State the blood parasite species.
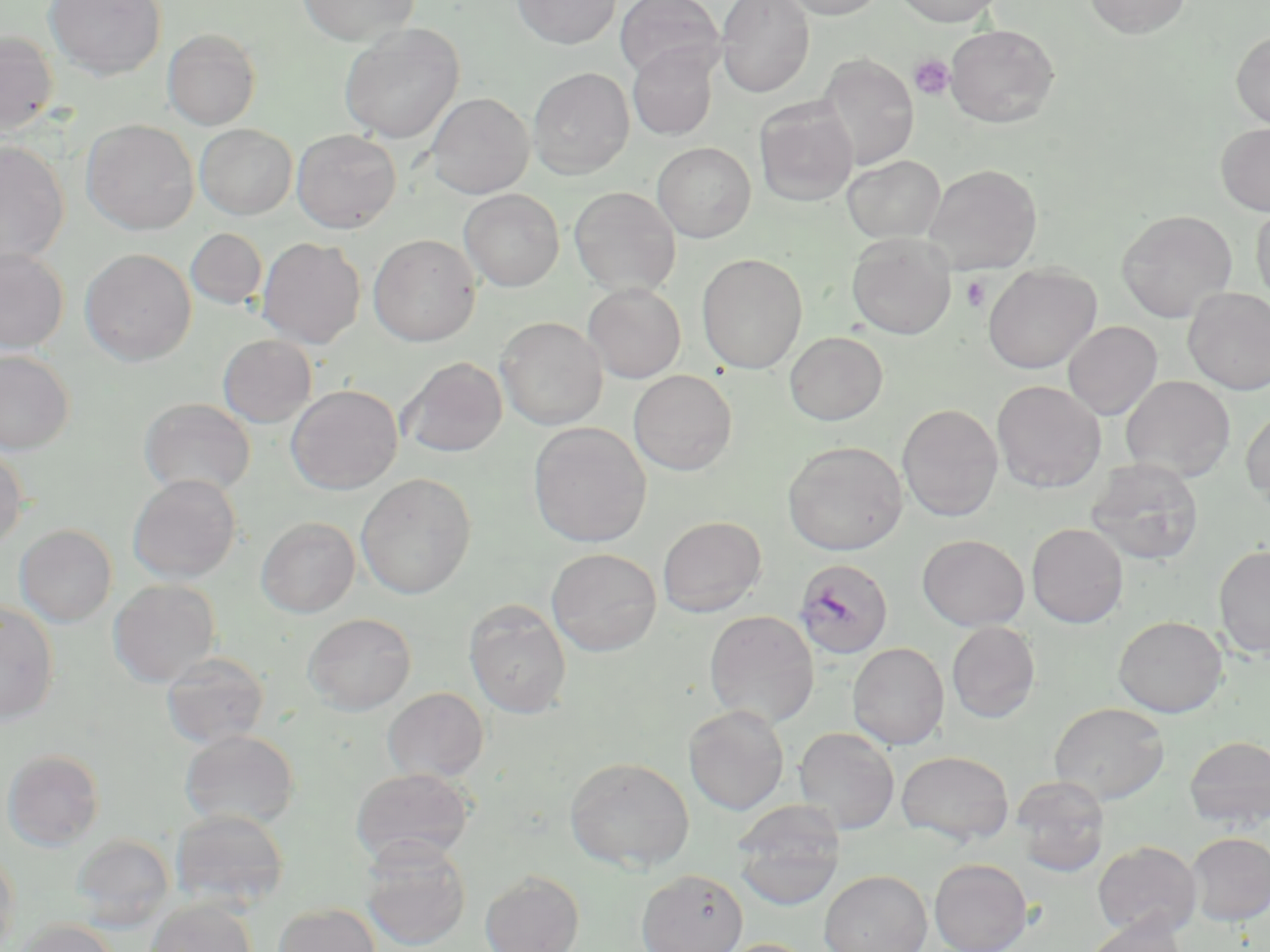

Plasmodium falciparum.

Approximate bounding boxes as (x1,y1)-(x2,y2) corner pairs in pixels. Plasmodium falciparum-infected red blood cell locations: (794,558)-(895,661). Platelet locations: (909,54)-(955,100), (961,275)-(991,313). Uninfected red blood cell locations: (44,0)-(166,80), (296,0)-(419,45), (513,0)-(620,49), (615,0)-(724,81), (715,0)-(815,97), (780,0)-(885,20), (894,0)-(1001,27), (1084,0)-(1192,38), (339,23)-(464,144), (944,24)-(1059,128), (163,28)-(261,130), (0,30)-(59,134), (1232,30)-(1270,129), (627,45)-(718,141), (815,54)-(920,170), (528,68)-(634,179), (426,92)-(534,199), (754,99)-(859,207), (81,119)-(199,235), (1216,122)-(1270,216), (195,124)-(297,220), (292,129)-(401,233), (0,140)-(69,265), (652,142)-(756,243), (843,155)-(945,242), (923,163)-(1042,274), (569,186)-(681,295), (459,189)-(564,292), (1251,200)-(1270,307), (1116,209)-(1237,322), (186,228)-(267,309), (846,233)-(957,339), (368,234)-(481,346), (256,236)-(366,348), (0,247)-(69,354), (80,248)-(197,365), (696,253)-(807,374), (983,263)-(1101,373), (583,283)-(686,383), (1184,287)-(1270,395), (496,316)-(607,430), (1063,321)-(1163,420), (784,331)-(888,425), (218,334)-(317,427), (0,349)-(74,454), (400,357)-(508,458), (628,370)-(737,475), (1120,375)-(1236,482), (992,380)-(1106,493), (286,384)-(403,494), (139,398)-(256,498), (897,404)-(1003,522), (1241,407)-(1270,509), (528,422)-(651,548), (782,440)-(907,556), (0,445)-(27,549), (1085,457)-(1204,566), (356,473)-(477,599), (127,474)-(242,583), (256,516)-(360,617), (657,516)-(766,617), (1027,523)-(1128,628), (14,524)-(117,627), (917,534)-(1029,631), (1214,544)-(1270,659), (547,548)-(662,656), (108,579)-(220,686), (464,600)-(571,719), (0,602)-(59,724), (703,610)-(820,728), (304,612)-(416,714), (1113,615)-(1228,717), (946,621)-(1040,723), (847,642)-(949,749), (160,651)-(270,750), (383,687)-(488,782), (1049,702)-(1169,804), (684,705)-(789,816), (793,727)-(900,834), (180,729)-(299,830), (1184,736)-(1270,830), (2,749)-(105,851), (895,750)-(1015,846), (564,756)-(695,872), (350,767)-(475,865), (1011,776)-(1110,876), (733,803)-(845,907), (170,808)-(290,912), (1186,832)-(1270,925), (71,834)-(175,930), (360,838)-(471,951), (1093,840)-(1202,940), (0,849)-(20,951), (929,858)-(1032,952), (637,869)-(748,952), (480,870)-(584,952), (819,870)-(932,952), (145,899)-(257,952), (274,903)-(381,952), (1083,918)-(1188,952), (16,919)-(118,952), (719,938)-(817,952). Captured at 1000x magnification. Thin blood film. Single field of view. Image is 1270×952 pixels. Light microscopy. May-Grünwald-Giemsa stain.